Outline each blood parasite and name the species.
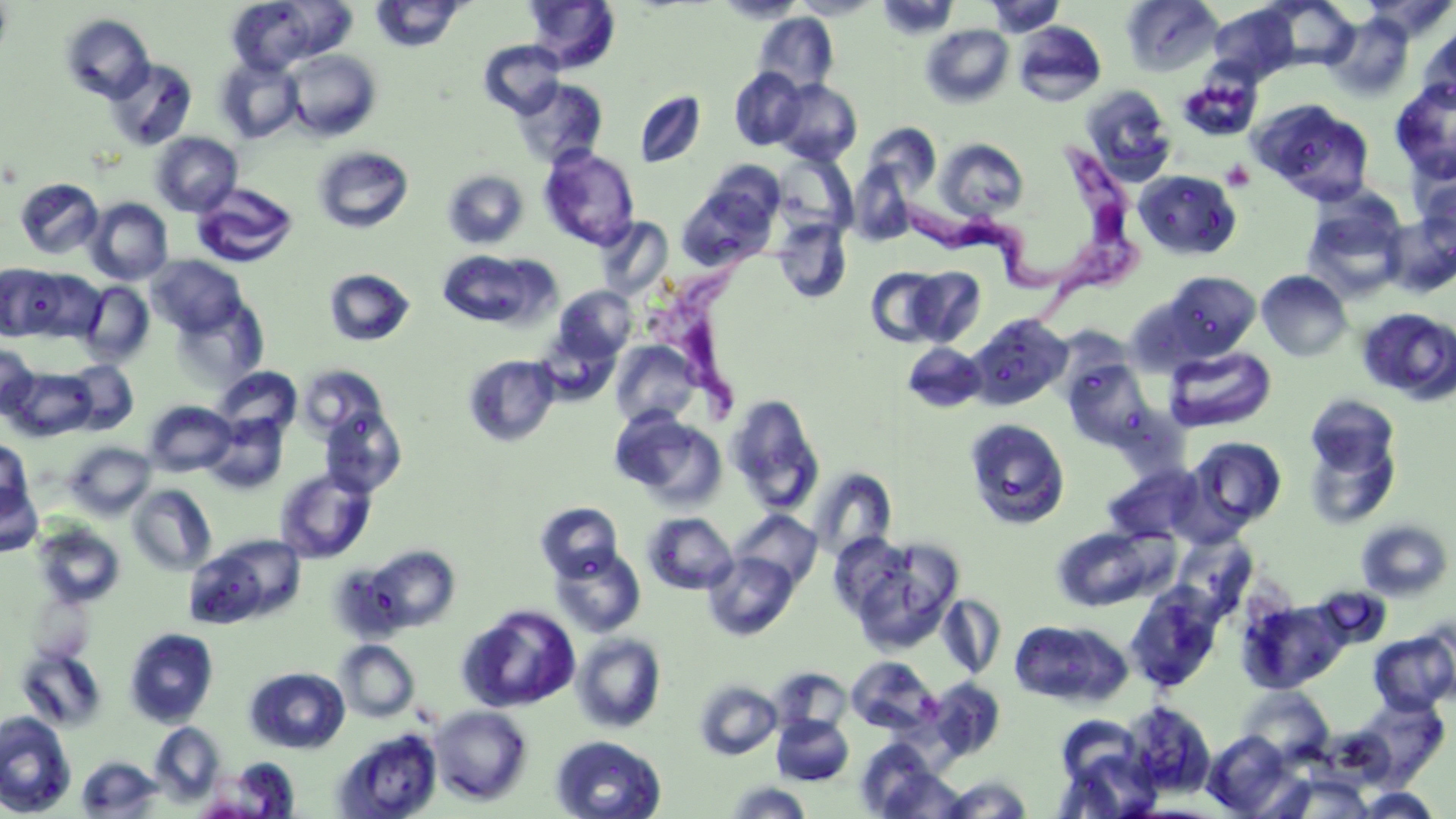
Approximate bounding boxes as (x1,y1)-(x2,y2) corner pairs in pixels.
Trypanosoma brucei: (1032,132)-(1152,336), (893,196)-(1089,285), (645,242)-(810,427).
No Plasmodium falciparum, Plasmodium ovale, Plasmodium malariae, Plasmodium vivax, or Babesia divergens observed.

slide-level diagnosis = Trypanosoma brucei
platelet locations = approximate bounding boxes as (x1,y1)-(x2,y2) corner pairs in pixels: (1220,160)-(1256,191)
preparation = thin blood smear
stain = May-Grünwald-Giemsa
image size = 1456×819 pixels
modality = light microscopy
uninfected red blood cell locations = approximate bounding boxes as (x1,y1)-(x2,y2) corner pairs in pixels: (0,0)-(13,69), (714,0)-(808,23), (789,0)-(883,19), (985,0)-(1065,38), (223,1)-(333,75), (266,1)-(359,60), (369,1)-(468,52), (525,1)-(620,72), (1121,1)-(1222,77), (876,2)-(958,42), (1206,4)-(1302,85), (1324,12)-(1415,103), (753,13)-(839,94), (60,14)-(155,103), (1421,22)-(1456,110), (1013,23)-(1106,106), (921,24)-(1014,108), (479,40)-(566,117), (282,49)-(382,141), (1182,55)-(1266,143), (214,56)-(303,143), (105,59)-(198,152), (730,68)-(807,151), (510,78)-(607,168), (1389,78)-(1456,183), (772,79)-(863,166), (1081,85)-(1176,182), (635,90)-(705,167), (1250,99)-(1375,204), (862,123)-(942,198), (151,132)-(243,215), (935,138)-(1029,220), (313,146)-(414,233), (539,146)-(640,250), (1409,151)-(1456,239), (771,153)-(856,237), (849,164)-(916,247), (441,169)-(530,250), (1133,169)-(1243,261), (15,179)-(103,260), (192,185)-(298,268), (1302,194)-(1410,300), (86,198)-(173,285), (1382,212)-(1456,298), (595,217)-(673,300), (772,219)-(852,304), (436,250)-(554,330), (148,255)-(247,338), (0,263)-(64,341), (866,267)-(949,348), (905,267)-(987,347), (324,268)-(415,347), (26,270)-(106,342), (1256,270)-(1352,361), (1161,271)-(1261,358), (78,281)-(153,366), (553,286)-(638,363), (173,295)-(268,392), (1357,307)-(1456,407), (967,314)-(1075,411), (610,341)-(701,427), (900,342)-(989,415), (0,344)-(39,418), (1163,346)-(1277,433), (463,354)-(560,448), (1062,358)-(1154,450), (63,361)-(138,434), (214,366)-(303,439), (296,366)-(386,442), (4,367)-(99,440), (726,395)-(825,514), (1303,400)-(1402,516), (144,401)-(236,476), (318,405)-(407,497), (611,411)-(726,507), (203,414)-(289,496), (964,418)-(1071,530), (1187,435)-(1287,532), (0,438)-(33,520), (65,442)-(156,519), (1103,464)-(1204,544), (276,468)-(375,564), (808,468)-(897,561), (0,482)-(42,557), (128,484)-(216,576), (535,503)-(624,581), (731,510)-(822,590), (643,512)-(738,594), (1355,519)-(1454,601), (32,524)-(126,608), (1051,526)-(1169,612), (829,532)-(943,636), (184,543)-(284,627), (362,545)-(461,633), (549,545)-(647,638), (703,551)-(799,641), (1126,588)-(1222,690), (935,596)-(1006,679), (1240,598)-(1349,694), (462,606)-(581,712), (1010,619)-(1132,707), (124,628)-(219,726), (1368,630)-(1456,715), (572,634)-(666,733), (336,640)-(419,722), (846,656)-(941,737), (245,667)-(350,754), (770,667)-(852,736), (694,680)-(782,760), (1357,695)-(1450,782), (1125,701)-(1215,795), (430,705)-(533,805), (0,711)-(76,816), (772,714)-(854,785), (150,723)-(226,804), (333,729)-(442,818), (1203,731)-(1293,816), (550,735)-(667,819), (853,739)-(950,818), (1056,746)-(1162,819), (76,756)-(165,817), (208,761)-(301,817), (1284,773)-(1371,817), (939,775)-(1033,818), (723,781)-(814,818), (1355,787)-(1443,818)
magnification = 1000x
field of view = one of a larger specimen